Classify the preparation.
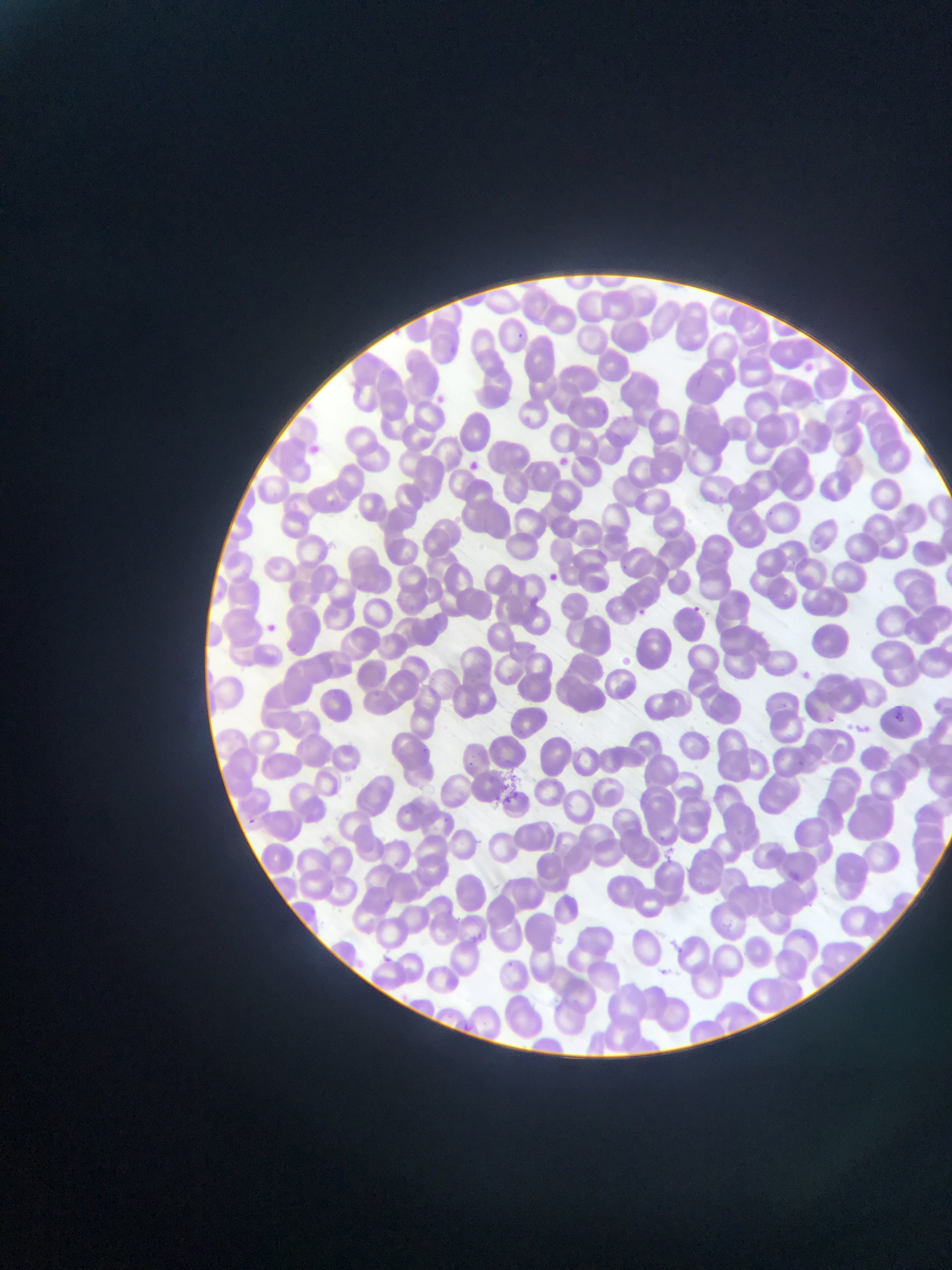

Thin blood smear.

field of view = single
capture = mobile-phone photograph through a microscope
image size = 952×1270 pixels
malaria parasite locations = approximate bounding boxes as (left, top, right, bottom) in pixels: (508, 328, 528, 346), (803, 362, 816, 375), (306, 442, 325, 459), (556, 455, 570, 468), (552, 457, 571, 474), (466, 459, 481, 473), (544, 571, 560, 586), (688, 603, 702, 616), (634, 605, 649, 619), (687, 605, 706, 622), (260, 619, 283, 639), (799, 668, 815, 682), (891, 710, 911, 730), (824, 713, 837, 724), (241, 816, 258, 831), (786, 868, 801, 886), (378, 953, 394, 966), (656, 966, 671, 980)
country = Ghana